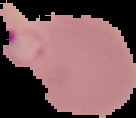
{
  "result": "Plasmodium parasites identified",
  "image_type": "segmented cell region on a black background",
  "image_size": "136×118 pixels",
  "preparation": "thin blood smear"
}